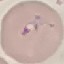

result = malaria parasites identified
stain = Giemsa
preparation = thin blood film
capture = smartphone through the microscope eyepiece
image type = automatically extracted cell patch, resized to 64 × 64 pixels